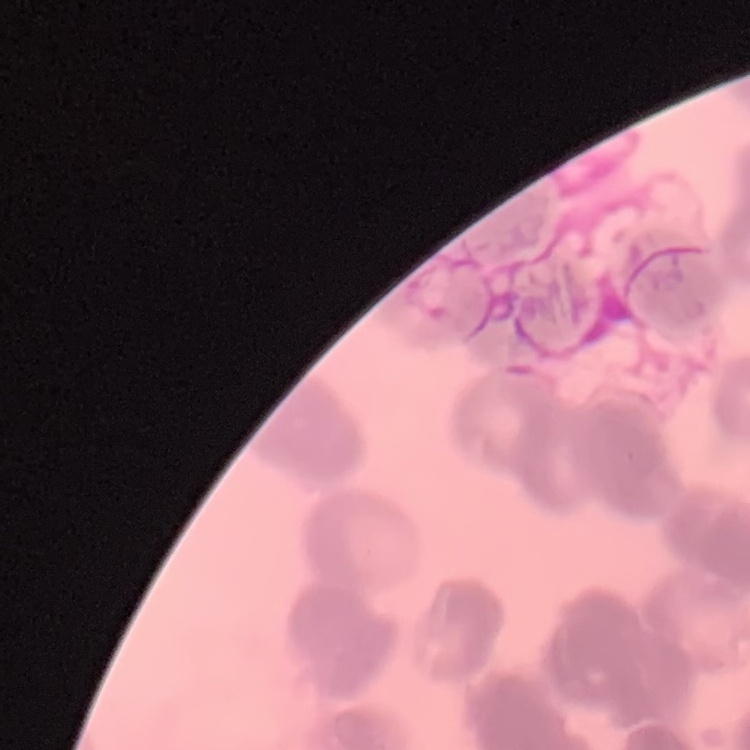 The erythrocytes show rouleaux formation. One tile cut from a larger photomicrograph. Field's or Giemsa stain. Thin peripheral smear.